Assess this cell for malaria.
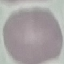

It is uninfected.

Summary:
  - Capture: smartphone through the microscope eyepiece
  - Image type: cell patch, automatically extracted from a larger field of view and resized to 64 × 64 pixels
  - Stain: Giemsa
  - Preparation: thin smear